Give the extent of all uninfected red blood cells.
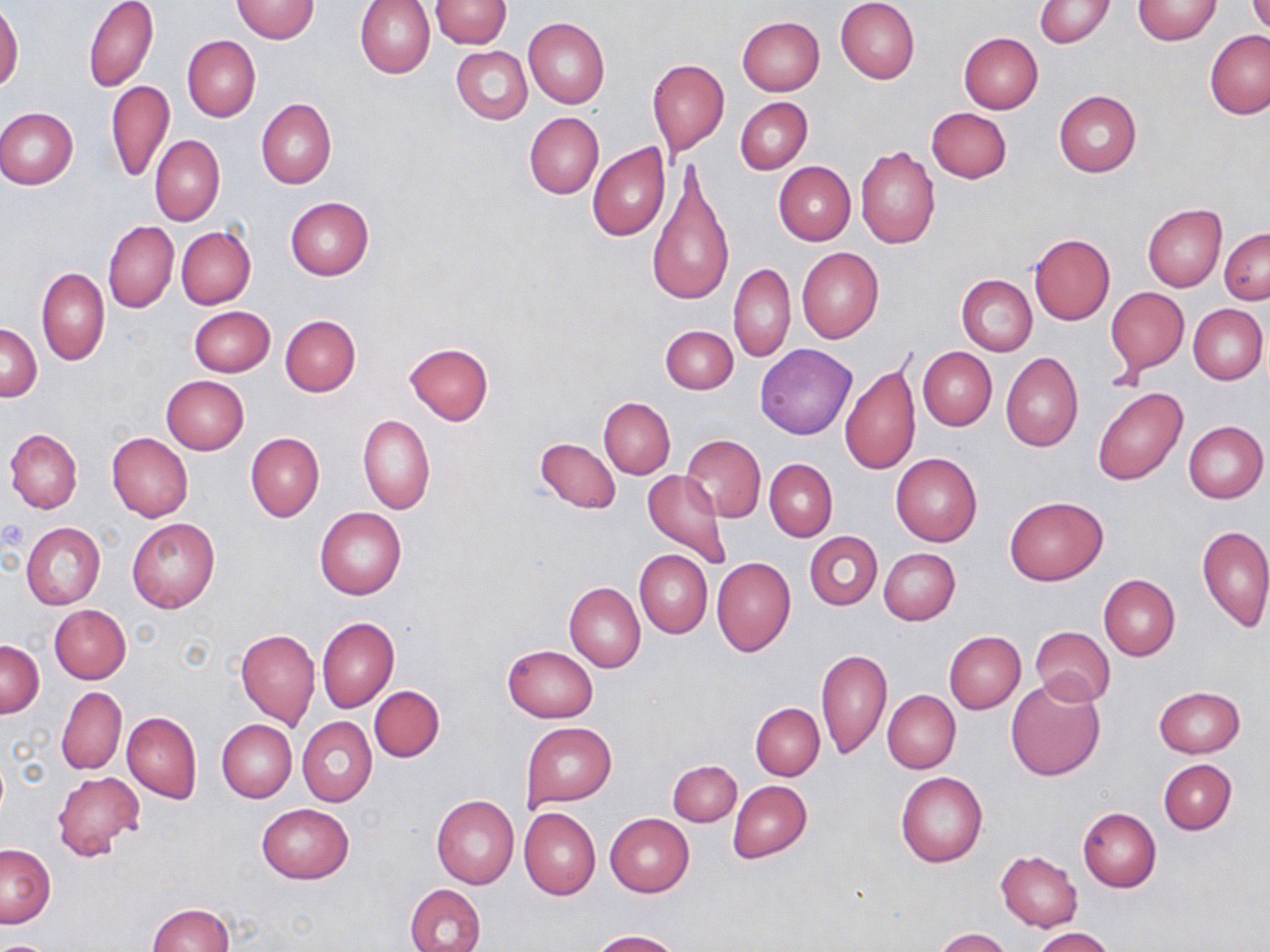

Approximate bounding boxes as (x1, y1, x2, y2) in pixels.
Uninfected red blood cells: (82, 0, 159, 92), (231, 0, 319, 43), (354, 0, 435, 79), (429, 0, 511, 48), (835, 0, 920, 84), (1133, 0, 1222, 43), (1034, 1, 1114, 48), (1248, 2, 1269, 35), (0, 5, 23, 93), (523, 17, 610, 108), (737, 17, 825, 95), (1206, 30, 1270, 119), (958, 33, 1044, 113), (182, 35, 260, 121), (452, 46, 532, 124), (647, 59, 729, 154), (107, 80, 174, 182), (1053, 90, 1142, 177), (735, 97, 812, 174), (257, 99, 336, 189), (926, 107, 1012, 183), (1, 108, 78, 189), (524, 113, 604, 199), (150, 135, 224, 225), (588, 143, 670, 243), (856, 145, 939, 249), (644, 162, 733, 310), (774, 162, 855, 245), (285, 196, 374, 280), (1143, 204, 1226, 292), (103, 221, 178, 314), (177, 226, 256, 310), (1220, 227, 1269, 304), (1028, 234, 1115, 326), (797, 248, 883, 343), (728, 262, 795, 363), (37, 267, 109, 365), (956, 275, 1036, 355), (1106, 287, 1189, 374), (1187, 304, 1267, 384), (188, 305, 275, 377), (280, 315, 360, 395), (1, 321, 42, 402), (660, 325, 738, 394), (405, 342, 493, 425), (754, 343, 856, 440), (917, 346, 996, 430), (1001, 352, 1084, 451), (840, 361, 921, 476), (161, 375, 249, 453), (1092, 387, 1188, 486), (599, 398, 675, 478), (357, 414, 434, 514), (1183, 421, 1267, 504), (4, 429, 82, 514), (106, 433, 192, 523), (246, 433, 325, 521), (682, 435, 766, 522), (535, 437, 621, 513), (891, 453, 983, 546), (765, 459, 836, 541), (643, 469, 734, 571), (1005, 496, 1107, 584), (314, 507, 407, 600), (127, 519, 220, 613), (21, 523, 105, 610), (1197, 524, 1269, 632), (805, 531, 882, 609), (879, 548, 959, 625), (635, 549, 712, 638), (711, 557, 795, 657), (1099, 574, 1180, 661), (565, 583, 645, 672), (50, 605, 130, 683), (317, 616, 398, 713), (1030, 627, 1115, 705), (236, 628, 319, 730), (944, 631, 1025, 713), (1, 640, 44, 716), (503, 645, 598, 723), (817, 647, 890, 759), (1005, 678, 1105, 781), (369, 686, 445, 762), (1153, 686, 1246, 758), (57, 687, 126, 776), (883, 691, 960, 774), (751, 703, 824, 780), (123, 713, 201, 802), (298, 717, 377, 806), (217, 720, 296, 801), (521, 723, 617, 809), (668, 759, 740, 826), (1159, 759, 1236, 835), (53, 770, 145, 863), (896, 772, 987, 867), (728, 781, 811, 862), (432, 795, 519, 888), (256, 805, 353, 884), (1078, 807, 1161, 892), (519, 808, 601, 900), (605, 814, 694, 897), (1, 843, 56, 927), (995, 851, 1081, 932), (406, 885, 485, 951), (146, 903, 234, 952), (1032, 927, 1115, 952), (933, 928, 1013, 952), (592, 930, 681, 952), (0, 938, 56, 952).

slide_level_diagnosis: no evidence of blood parasites
stain: May-Grünwald-Giemsa
preparation: thin blood smear
image_size: 1270×952 pixels
modality: light microscopy
magnification: 1000x
field_of_view: one of a larger specimen